Name the parasite shown.
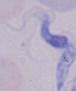

This is a trypanosome.

{
  "magnification": "1000x",
  "modality": "photomicrograph"
}